Classify this cell by malaria status.
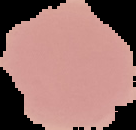
Uninfected.

image type = segmented cell region on a black background
image size = 136×130 pixels
preparation = thin blood film